Comment on the morphology of the red blood cells.
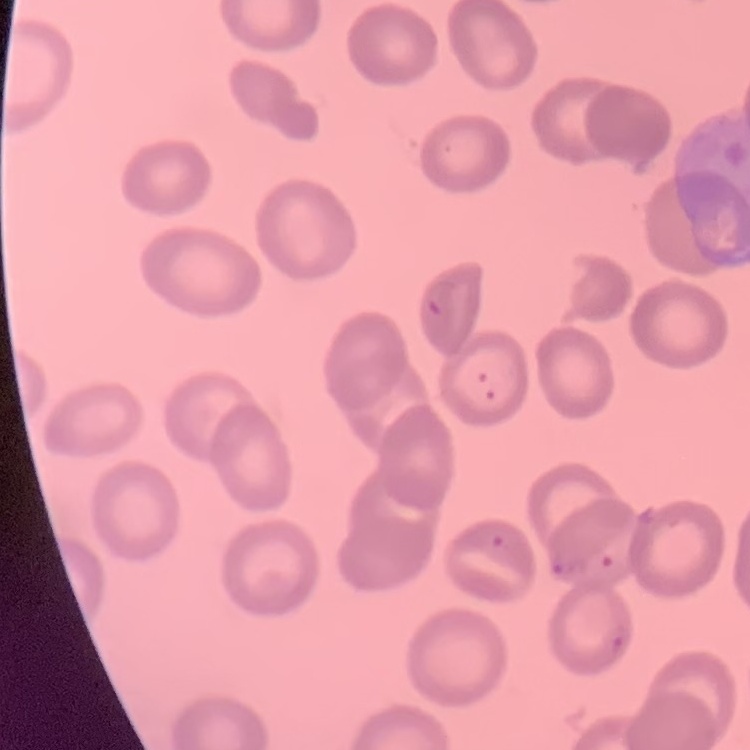
They show no rouleaux formation.

preparation = thin blood smear
image type = one tile cut from a larger photomicrograph
stain = Field's or Giemsa